Assess this cell for malaria.
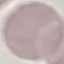

Uninfected.

Summary:
  - Preparation: thin blood smear
  - Stain: Giemsa
  - Capture: smartphone through the microscope eyepiece
  - Image type: cell patch, automatically extracted from a larger field of view and resized to 64 × 64 pixels